Assess the morphology of the red blood cells.
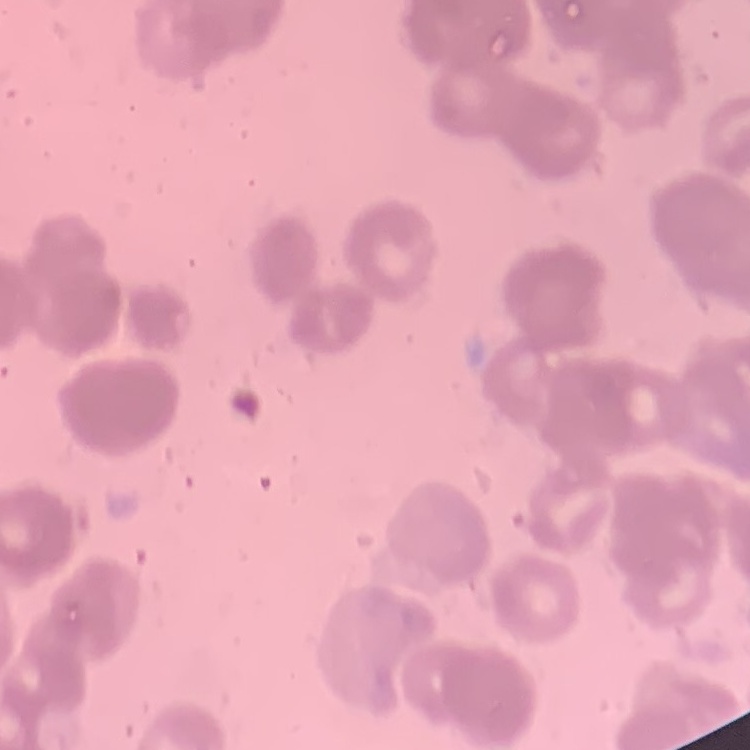
They show rouleaux formation.

image_type: square crop of a larger photomicrograph
stain: Field's or Giemsa
preparation: thin blood film